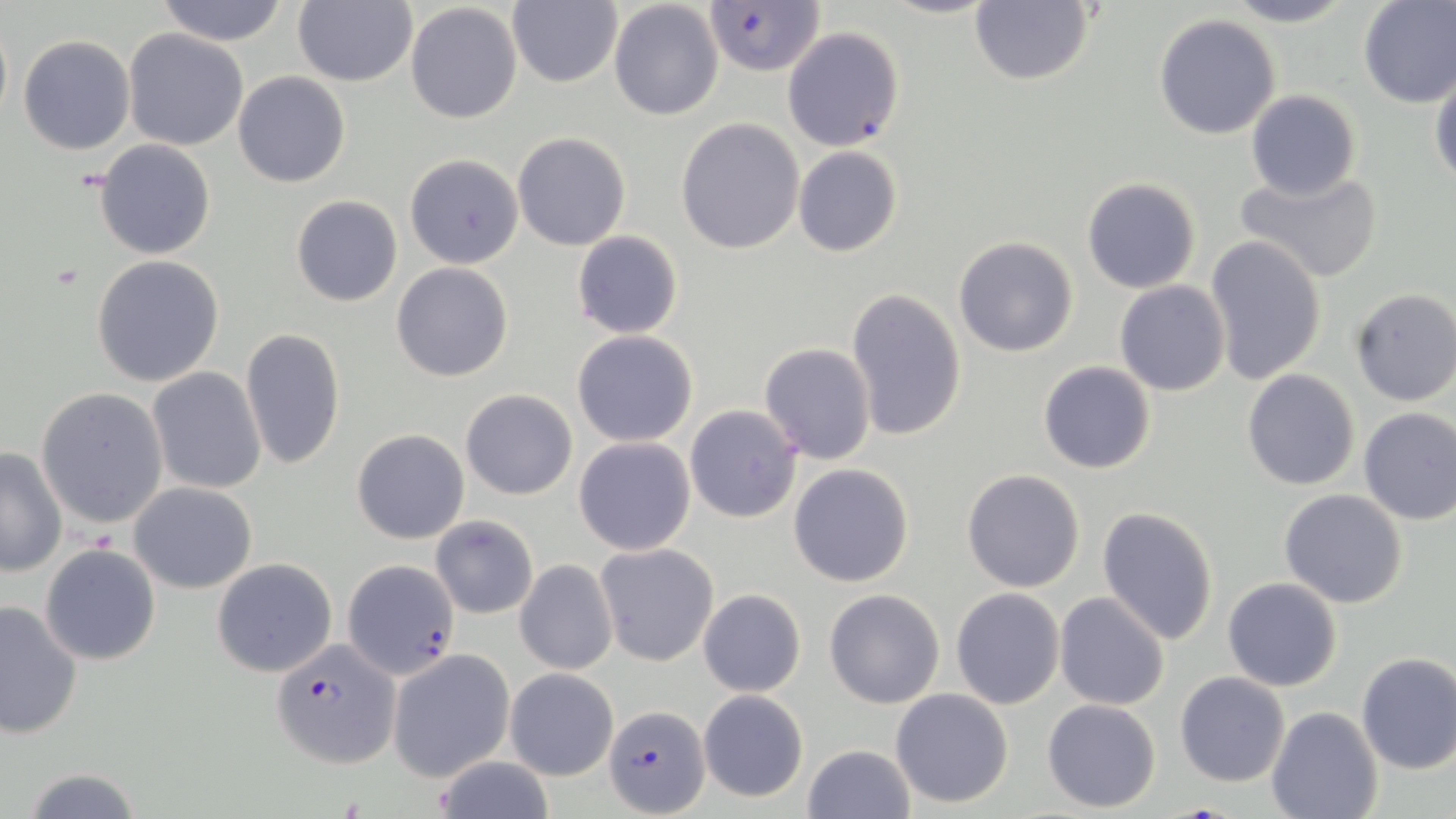

Summary:
  - Coordinate format: approximate bounding boxes as [x1, y1, x2, y2] in pixels
  - Uninfected red blood cell locations: [155, 0, 292, 45], [293, 0, 417, 87], [877, 0, 1003, 19], [1222, 0, 1355, 27], [1357, 0, 1456, 107], [505, 1, 623, 88], [608, 1, 723, 120], [405, 2, 523, 123], [968, 2, 1094, 86], [1153, 13, 1282, 139], [0, 14, 12, 130], [782, 26, 905, 152], [123, 28, 249, 151], [19, 34, 135, 155], [1430, 67, 1456, 187], [232, 71, 350, 188], [1244, 89, 1361, 202], [676, 117, 805, 254], [512, 131, 631, 251], [94, 139, 215, 259], [793, 145, 903, 257], [403, 154, 524, 269], [1236, 165, 1383, 283], [1082, 177, 1201, 293], [291, 195, 403, 307], [571, 231, 685, 339], [952, 235, 1079, 357], [1205, 235, 1328, 384], [92, 256, 224, 389], [391, 263, 514, 382], [1115, 281, 1231, 397], [844, 287, 966, 443], [1349, 287, 1456, 406], [241, 326, 347, 473], [572, 329, 698, 447], [759, 342, 877, 464], [1038, 361, 1157, 475], [148, 368, 267, 495], [1242, 369, 1361, 491], [36, 388, 169, 528], [460, 389, 578, 500], [685, 405, 803, 523], [1356, 406, 1456, 526], [352, 429, 470, 544], [573, 435, 696, 555], [0, 445, 67, 578], [788, 462, 915, 587], [961, 468, 1086, 593], [128, 483, 258, 594], [1278, 489, 1408, 609], [1096, 506, 1220, 648], [431, 516, 539, 619], [594, 542, 719, 667], [40, 544, 162, 665], [212, 558, 339, 678], [515, 560, 618, 674], [1222, 576, 1343, 691], [698, 588, 805, 697], [950, 588, 1066, 710], [823, 589, 945, 709], [1054, 592, 1171, 710], [0, 599, 83, 740], [388, 649, 514, 781], [1356, 652, 1455, 775], [505, 668, 618, 781], [1175, 671, 1290, 787], [889, 688, 1016, 809], [697, 689, 809, 803], [1041, 699, 1162, 812], [1266, 706, 1383, 819], [802, 743, 915, 819], [431, 751, 555, 819], [18, 766, 147, 819]
  - Plasmodium falciparum-infected red blood cell locations: [702, 1, 827, 78], [342, 560, 459, 680], [271, 641, 400, 768], [605, 703, 710, 817]
  - Slide-level diagnosis: Plasmodium falciparum
  - Magnification: 1000x
  - Image size: 1456×819 pixels
  - Stain: May-Grünwald-Giemsa
  - Preparation: thin blood film
  - Field of view: single
  - Modality: optical microscopy